State which cell type is depicted.
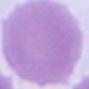

This is an erythrocyte.

Summary:
  - Magnification: 1000x
  - Modality: micrograph